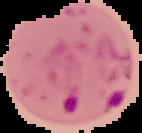

Summary:
  - Result: Plasmodium parasites identified
  - Preparation: thin blood film
  - Image type: cell region segmented out of the field of view; surrounding area masked to black
  - Image size: 142×133 pixels